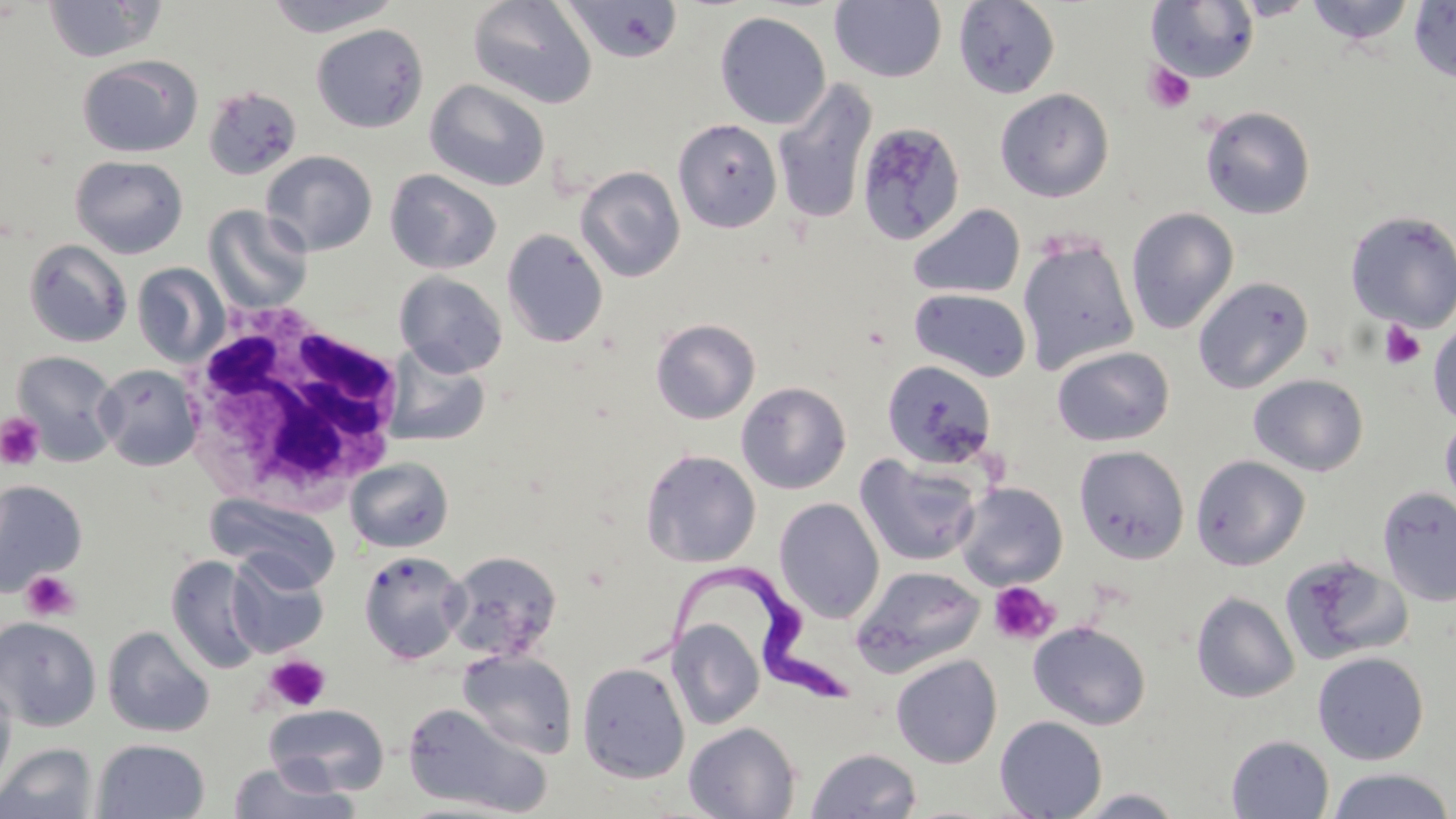
Summary:
  - Coordinate format: approximate bounding boxes as named x1/y1/x2/y2 corners in pixels
  - Uninfected red blood cell locations: (x1=42, y1=0, x2=165, y2=63), (x1=265, y1=0, x2=401, y2=37), (x1=467, y1=0, x2=597, y2=109), (x1=562, y1=0, x2=684, y2=63), (x1=953, y1=0, x2=1060, y2=98), (x1=1304, y1=0, x2=1417, y2=46), (x1=830, y1=1, x2=947, y2=82), (x1=1409, y1=1, x2=1456, y2=83), (x1=1146, y1=2, x2=1259, y2=84), (x1=714, y1=11, x2=831, y2=130), (x1=310, y1=23, x2=429, y2=133), (x1=76, y1=54, x2=203, y2=158), (x1=772, y1=78, x2=878, y2=226), (x1=425, y1=79, x2=550, y2=192), (x1=202, y1=85, x2=303, y2=181), (x1=995, y1=87, x2=1114, y2=202), (x1=1200, y1=105, x2=1316, y2=219), (x1=673, y1=118, x2=782, y2=233), (x1=855, y1=122, x2=966, y2=245), (x1=261, y1=151, x2=377, y2=256), (x1=70, y1=155, x2=189, y2=258), (x1=575, y1=166, x2=685, y2=283), (x1=385, y1=169, x2=502, y2=274), (x1=907, y1=203, x2=1025, y2=299), (x1=204, y1=204, x2=313, y2=313), (x1=1125, y1=207, x2=1239, y2=335), (x1=1344, y1=210, x2=1456, y2=332), (x1=501, y1=227, x2=608, y2=348), (x1=1018, y1=235, x2=1139, y2=376), (x1=23, y1=239, x2=133, y2=347), (x1=132, y1=263, x2=230, y2=367), (x1=395, y1=271, x2=507, y2=377), (x1=1193, y1=276, x2=1314, y2=393), (x1=909, y1=288, x2=1032, y2=382), (x1=651, y1=318, x2=760, y2=424), (x1=1428, y1=319, x2=1456, y2=425), (x1=1052, y1=345, x2=1174, y2=447), (x1=384, y1=347, x2=492, y2=448), (x1=11, y1=351, x2=121, y2=466), (x1=881, y1=359, x2=999, y2=470), (x1=96, y1=363, x2=202, y2=471), (x1=1248, y1=374, x2=1368, y2=476), (x1=736, y1=381, x2=851, y2=494), (x1=1440, y1=412, x2=1456, y2=513), (x1=1074, y1=445, x2=1190, y2=563), (x1=640, y1=448, x2=761, y2=568), (x1=855, y1=453, x2=983, y2=567), (x1=1191, y1=455, x2=1310, y2=570), (x1=345, y1=457, x2=453, y2=553), (x1=0, y1=480, x2=87, y2=597), (x1=954, y1=482, x2=1068, y2=590), (x1=1378, y1=485, x2=1456, y2=607), (x1=208, y1=494, x2=342, y2=591), (x1=773, y1=497, x2=885, y2=623), (x1=358, y1=550, x2=468, y2=663), (x1=442, y1=550, x2=563, y2=663), (x1=226, y1=553, x2=329, y2=657), (x1=1281, y1=554, x2=1413, y2=665), (x1=166, y1=555, x2=265, y2=673), (x1=851, y1=565, x2=986, y2=676), (x1=1191, y1=590, x2=1300, y2=703), (x1=0, y1=617, x2=101, y2=732), (x1=666, y1=618, x2=765, y2=730), (x1=1028, y1=620, x2=1151, y2=730), (x1=102, y1=626, x2=215, y2=738), (x1=458, y1=649, x2=578, y2=759), (x1=1312, y1=651, x2=1429, y2=765), (x1=890, y1=653, x2=1002, y2=768), (x1=576, y1=662, x2=690, y2=784), (x1=0, y1=676, x2=16, y2=796), (x1=402, y1=702, x2=551, y2=816), (x1=263, y1=704, x2=390, y2=796), (x1=995, y1=715, x2=1107, y2=819), (x1=684, y1=722, x2=801, y2=818), (x1=1225, y1=734, x2=1334, y2=818), (x1=92, y1=738, x2=210, y2=819), (x1=0, y1=743, x2=97, y2=819), (x1=806, y1=747, x2=922, y2=819), (x1=227, y1=762, x2=358, y2=819), (x1=1326, y1=767, x2=1456, y2=819)
  - Trypanosoma brucei locations: (x1=634, y1=562, x2=853, y2=707)
  - White blood cell locations: (x1=178, y1=303, x2=410, y2=508)
  - Platelet locations: (x1=1142, y1=61, x2=1195, y2=113), (x1=1378, y1=321, x2=1427, y2=369), (x1=0, y1=413, x2=45, y2=470), (x1=21, y1=570, x2=81, y2=621), (x1=988, y1=581, x2=1059, y2=645), (x1=263, y1=654, x2=330, y2=712)
  - Slide-level diagnosis: Trypanosoma brucei
  - Preparation: thin blood film
  - Field of view: single
  - Magnification: 1000x
  - Modality: light microscopy
  - Image size: 1456×819 pixels
  - Stain: May-Grünwald-Giemsa